Locate every blood parasite and identify its species.
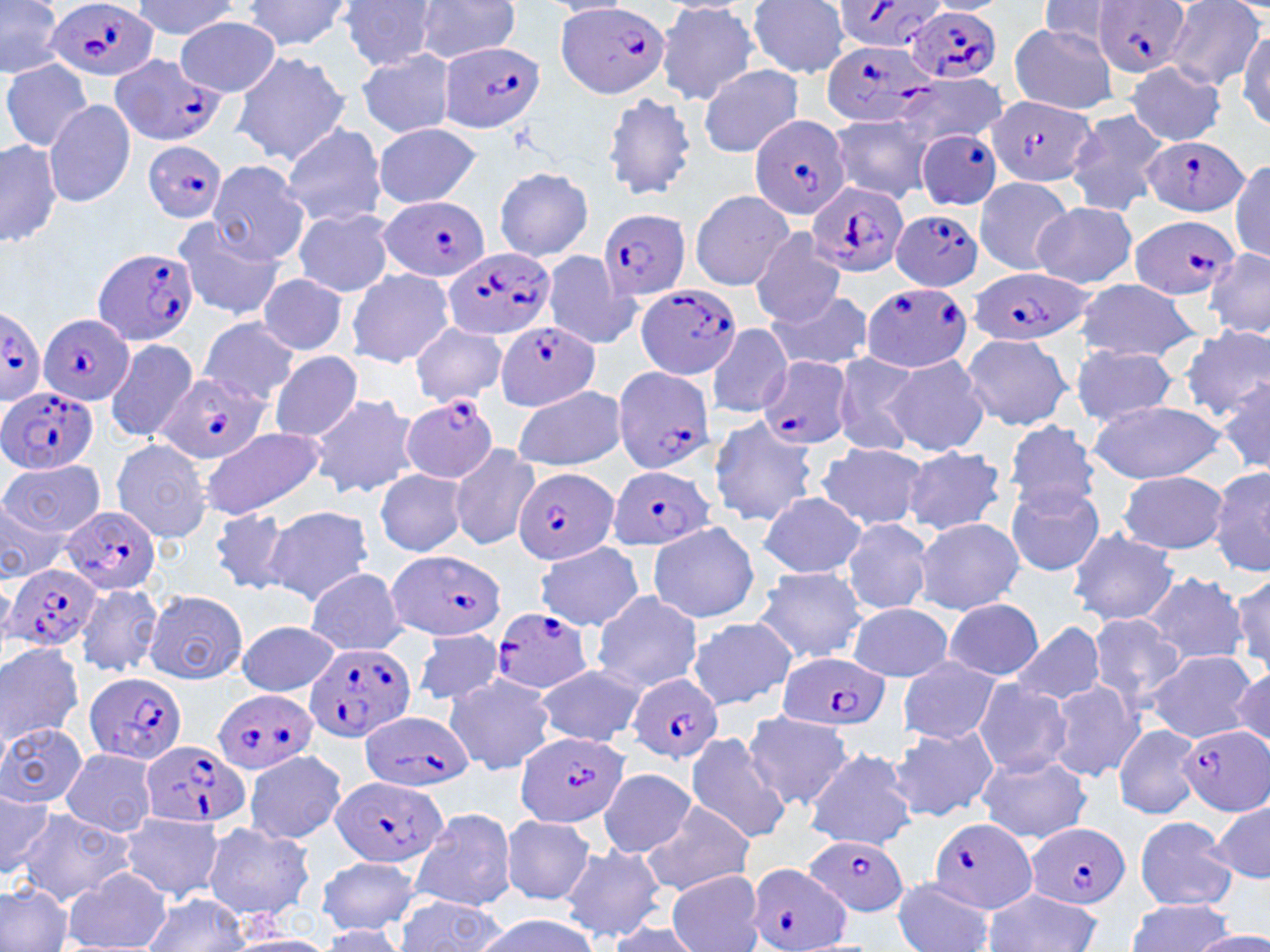

Approximate bounding boxes as [x1, y1, x2, y2] in pixels.
Plasmodium falciparum-infected red blood cells: [46, 0, 159, 83], [1096, 0, 1190, 77], [831, 2, 952, 55], [556, 4, 671, 99], [908, 5, 1005, 86], [822, 38, 934, 131], [436, 40, 546, 135], [109, 54, 224, 146], [987, 95, 1096, 189], [748, 114, 852, 220], [915, 129, 1003, 211], [1141, 134, 1251, 217], [142, 139, 229, 222], [808, 182, 910, 280], [380, 196, 490, 283], [598, 209, 691, 302], [888, 209, 987, 291], [1127, 215, 1239, 301], [93, 245, 200, 345], [442, 246, 556, 342], [967, 270, 1093, 348], [860, 282, 973, 373], [636, 285, 743, 380], [0, 307, 46, 401], [40, 312, 133, 407], [497, 321, 601, 410], [757, 356, 853, 451], [612, 365, 713, 475], [157, 372, 272, 465], [0, 387, 97, 474], [402, 395, 500, 485], [513, 466, 618, 567], [608, 466, 712, 551], [61, 507, 159, 594], [389, 549, 508, 643], [5, 564, 102, 652], [489, 608, 593, 696], [303, 641, 419, 742], [777, 652, 888, 733], [86, 672, 186, 767], [628, 673, 723, 763], [211, 690, 316, 776], [360, 711, 473, 794], [1178, 725, 1269, 816], [515, 731, 628, 830], [141, 740, 251, 832], [331, 776, 447, 867], [926, 816, 1037, 916], [1024, 822, 1131, 908], [804, 833, 911, 919], [748, 863, 853, 952].
No Plasmodium ovale, Plasmodium malariae, Plasmodium vivax, Babesia divergens, or Trypanosoma brucei observed.

Uninfected red blood cell locations: [0, 0, 65, 79], [132, 0, 237, 39], [240, 0, 355, 52], [340, 0, 438, 69], [922, 0, 1009, 16], [1164, 0, 1265, 93], [543, 1, 637, 18], [746, 1, 850, 77], [1037, 1, 1127, 50], [411, 2, 524, 65], [654, 3, 760, 106], [175, 15, 282, 96], [1009, 23, 1119, 113], [1237, 26, 1270, 130], [355, 49, 458, 139], [230, 50, 351, 165], [1, 59, 93, 150], [1124, 61, 1225, 144], [698, 64, 803, 158], [895, 73, 1006, 149], [602, 91, 698, 202], [44, 99, 135, 207], [1063, 107, 1172, 218], [834, 113, 939, 199], [280, 123, 386, 227], [372, 124, 483, 207], [0, 137, 62, 252], [1230, 158, 1270, 261], [207, 160, 311, 265], [493, 166, 594, 263], [973, 176, 1079, 275], [689, 189, 797, 292], [1031, 201, 1138, 289], [291, 208, 394, 298], [170, 216, 286, 321], [750, 228, 847, 326], [1204, 247, 1270, 341], [539, 251, 642, 351], [346, 268, 455, 367], [256, 275, 351, 357], [1072, 280, 1204, 362], [765, 288, 873, 372], [198, 317, 300, 407], [409, 323, 507, 406], [705, 323, 793, 420], [1180, 326, 1270, 421], [960, 331, 1076, 431], [103, 337, 199, 444], [1068, 346, 1182, 425], [269, 350, 365, 442], [830, 352, 923, 456], [885, 354, 989, 455], [1216, 373, 1270, 475], [513, 384, 628, 471], [307, 392, 419, 498], [1087, 397, 1229, 483], [706, 415, 820, 526], [1003, 419, 1100, 515], [197, 427, 325, 520], [109, 438, 215, 543], [816, 442, 930, 532], [448, 443, 541, 551], [901, 445, 1007, 536], [2, 458, 105, 539], [1209, 461, 1270, 580], [374, 470, 470, 556], [1118, 471, 1229, 554], [1004, 481, 1105, 578], [759, 491, 866, 578], [0, 498, 65, 583], [208, 505, 294, 595], [263, 505, 374, 604], [914, 517, 1026, 614], [840, 519, 933, 615], [646, 521, 761, 625], [1067, 528, 1179, 628], [535, 542, 642, 630], [304, 567, 408, 655], [753, 567, 868, 665], [1141, 569, 1249, 668], [1229, 570, 1270, 674], [75, 581, 163, 676], [143, 590, 248, 684], [590, 590, 703, 692], [943, 599, 1045, 681], [847, 603, 955, 681], [1088, 613, 1186, 707], [686, 616, 798, 711], [237, 620, 342, 698], [1010, 622, 1108, 708], [411, 631, 507, 706], [0, 642, 84, 745], [1144, 650, 1259, 742], [897, 658, 1000, 743], [534, 666, 646, 746], [1232, 666, 1269, 751], [442, 672, 555, 775], [1047, 679, 1146, 783], [973, 680, 1073, 779], [741, 711, 857, 810], [0, 722, 89, 808], [1113, 723, 1203, 820], [887, 724, 997, 822], [684, 731, 793, 844], [803, 748, 918, 851], [60, 750, 160, 835], [243, 750, 348, 844], [976, 753, 1090, 842], [598, 767, 698, 858], [0, 785, 55, 881], [640, 797, 756, 897], [1211, 801, 1269, 886], [410, 806, 517, 911], [12, 810, 135, 904], [118, 813, 227, 901], [502, 815, 598, 905], [1133, 817, 1237, 910], [202, 823, 316, 924], [558, 845, 667, 943], [314, 855, 422, 933], [64, 866, 173, 952], [667, 869, 765, 952], [893, 877, 997, 951], [0, 884, 74, 952], [979, 888, 1105, 952], [138, 894, 252, 951], [393, 900, 509, 951], [1125, 900, 1237, 951], [472, 914, 599, 952], [603, 919, 704, 952], [317, 926, 405, 950], [1192, 930, 1270, 952], [227, 934, 341, 952]. Slide-level diagnosis: Plasmodium falciparum. Optical microscopy. 1000x magnification. Single field of view. May-Grünwald-Giemsa stain. Image is 1270×952 pixels. Thin blood smear.